Assess this cell for malaria.
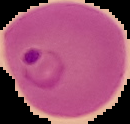
It is parasitized.

Image is 130×124 pixels. From a thin blood smear. The area outside the segmented cell region is set to black.